Classify this cell by malaria status.
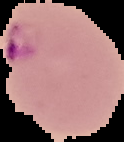

It is parasitized.

preparation = thin blood film
image type = segmented cell region on a black background
image size = 124×142 pixels